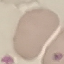

Summary:
  - Malaria status: uninfected
  - Image type: automatically extracted cell patch, resized to 64 × 64 pixels
  - Stain: Giemsa
  - Capture: smartphone through the microscope eyepiece
  - Preparation: thin smear